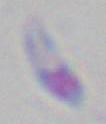

magnification: 1000x
identification: Toxoplasma gondii
modality: photomicrograph